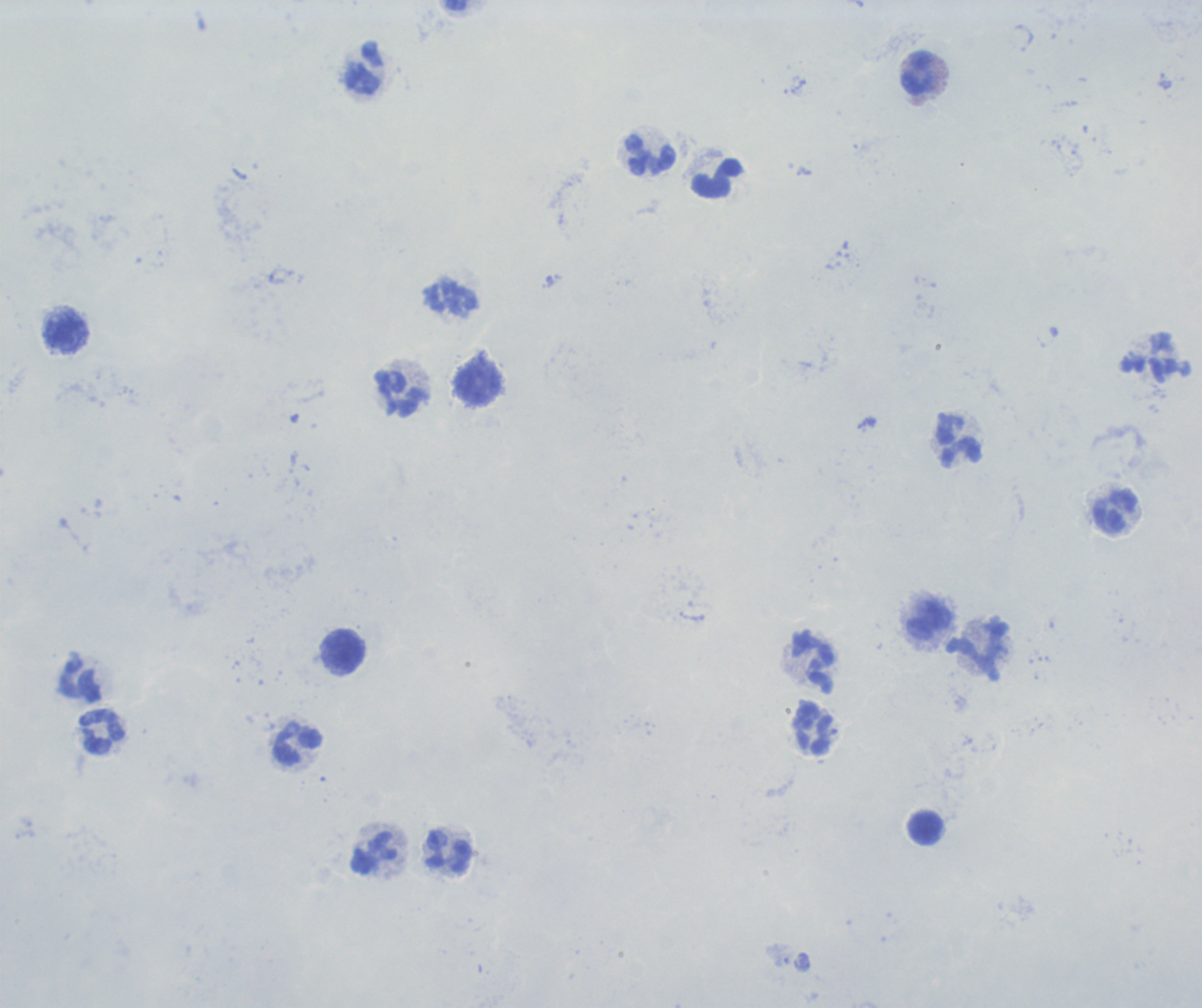
coordinate format = approximate centers as (x, y) in pixels
leukocyte locations = (365, 69), (919, 73), (651, 155), (718, 179), (67, 333), (478, 383), (401, 394), (960, 442), (1115, 511), (929, 619), (344, 652), (979, 652), (814, 662), (81, 681), (815, 729), (102, 732), (298, 745), (925, 828), (448, 853), (374, 854)
result = no malaria parasites seen
image size = 1202×1008 pixels
magnification = 100x
context = previously used in a real diagnosis
preparation = thick blood film
field of view = single
stain = Romanowsky
background quality = poor